Locate every Plasmodium ovale-infected red blood cell.
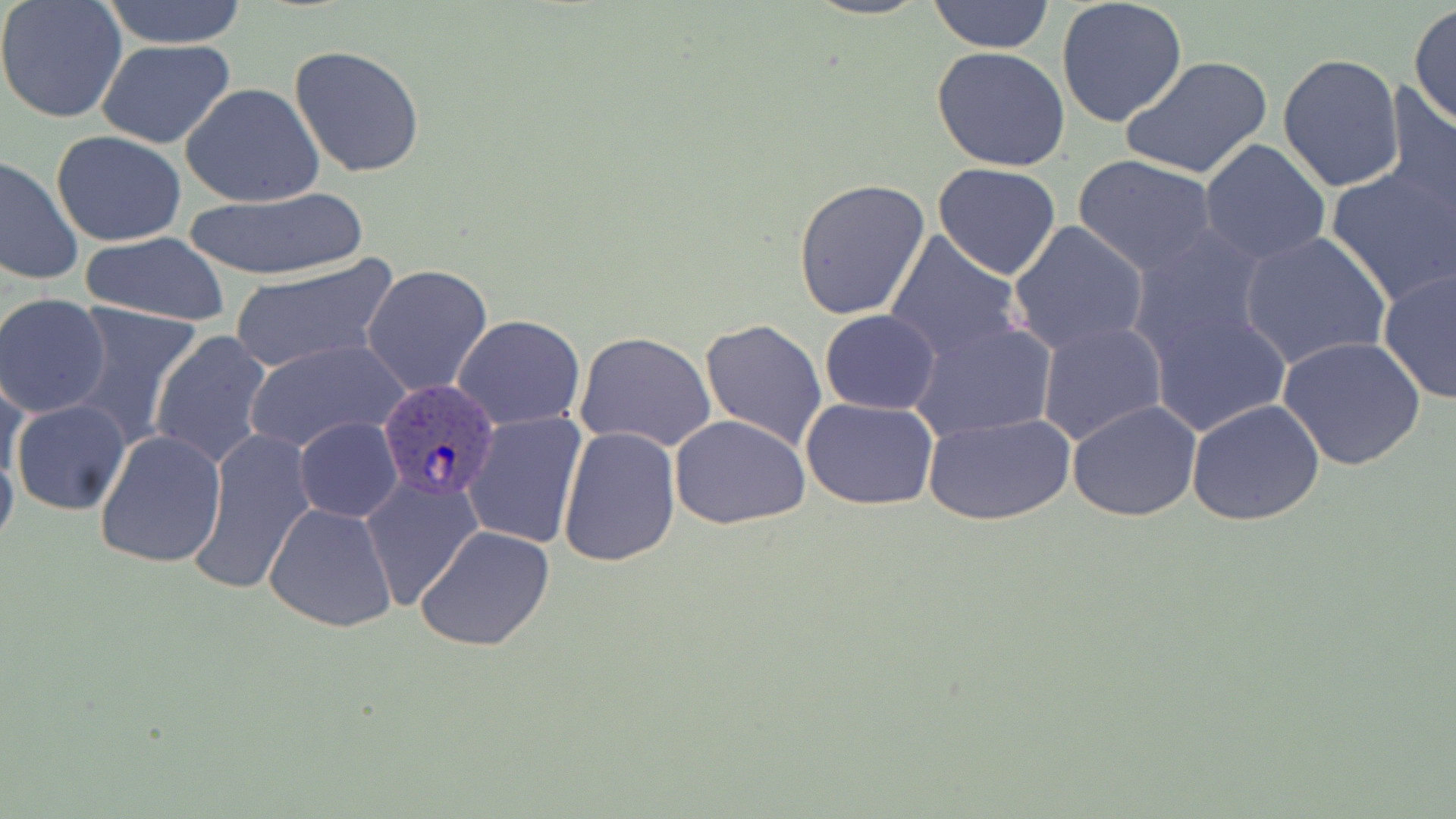
Approximate bounding boxes as (x1,y1)-(x2,y2) corner pairs in pixels.
Plasmodium ovale-infected red blood cells: (375,376)-(499,501).

Summary:
  - Uninfected red blood cell locations: (0,0)-(128,122), (927,0)-(1055,53), (1056,0)-(1189,126), (96,1)-(251,49), (1408,5)-(1455,130), (96,41)-(240,147), (287,44)-(427,180), (932,47)-(1071,172), (1278,53)-(1404,193), (1118,55)-(1272,182), (1382,82)-(1455,220), (181,83)-(326,208), (51,131)-(187,245), (1199,139)-(1331,267), (0,155)-(82,287), (1072,156)-(1218,277), (932,163)-(1061,281), (1326,164)-(1456,307), (791,179)-(933,322), (185,190)-(368,279), (1007,220)-(1151,356), (882,231)-(1027,366), (1125,231)-(1278,405), (1237,231)-(1392,371), (78,232)-(234,326), (228,255)-(400,374), (362,264)-(494,396), (1378,267)-(1456,406), (0,293)-(113,419), (66,302)-(203,445), (1145,302)-(1290,438), (819,309)-(942,415), (452,314)-(586,429), (699,317)-(829,452), (1036,321)-(1168,447), (912,322)-(1057,440), (149,331)-(273,471), (574,332)-(715,453), (1278,335)-(1427,471), (243,337)-(410,455), (1,367)-(29,498), (801,397)-(940,510), (1186,398)-(1326,526), (10,399)-(131,516), (1067,399)-(1202,520), (462,412)-(588,550), (922,412)-(1073,526), (670,414)-(810,530), (295,418)-(402,522), (557,425)-(681,568), (184,428)-(315,597), (94,429)-(226,568), (360,475)-(486,611), (264,502)-(398,633), (414,524)-(557,653)
  - Slide-level diagnosis: Plasmodium ovale
  - Image size: 1456×819 pixels
  - Stain: May-Grünwald-Giemsa
  - Field of view: single
  - Preparation: thin blood smear
  - Magnification: 1000x
  - Modality: light microscopy